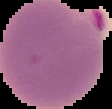

Segmented cell region on a black background. Image is 112×109 pixels. From a thin blood smear. Result: Plasmodium parasites detected.